State which cell type is depicted.
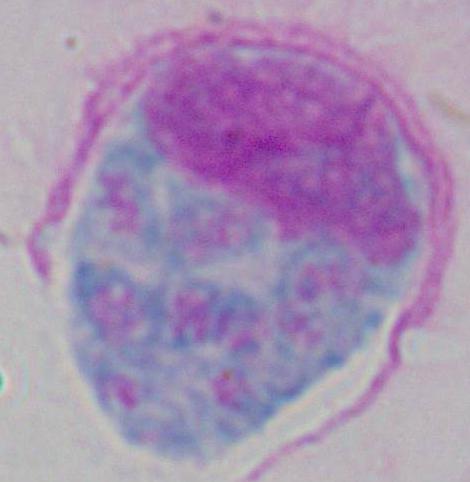

This is a leukocyte.

Summary:
  - Magnification: 1000x
  - Modality: micrograph